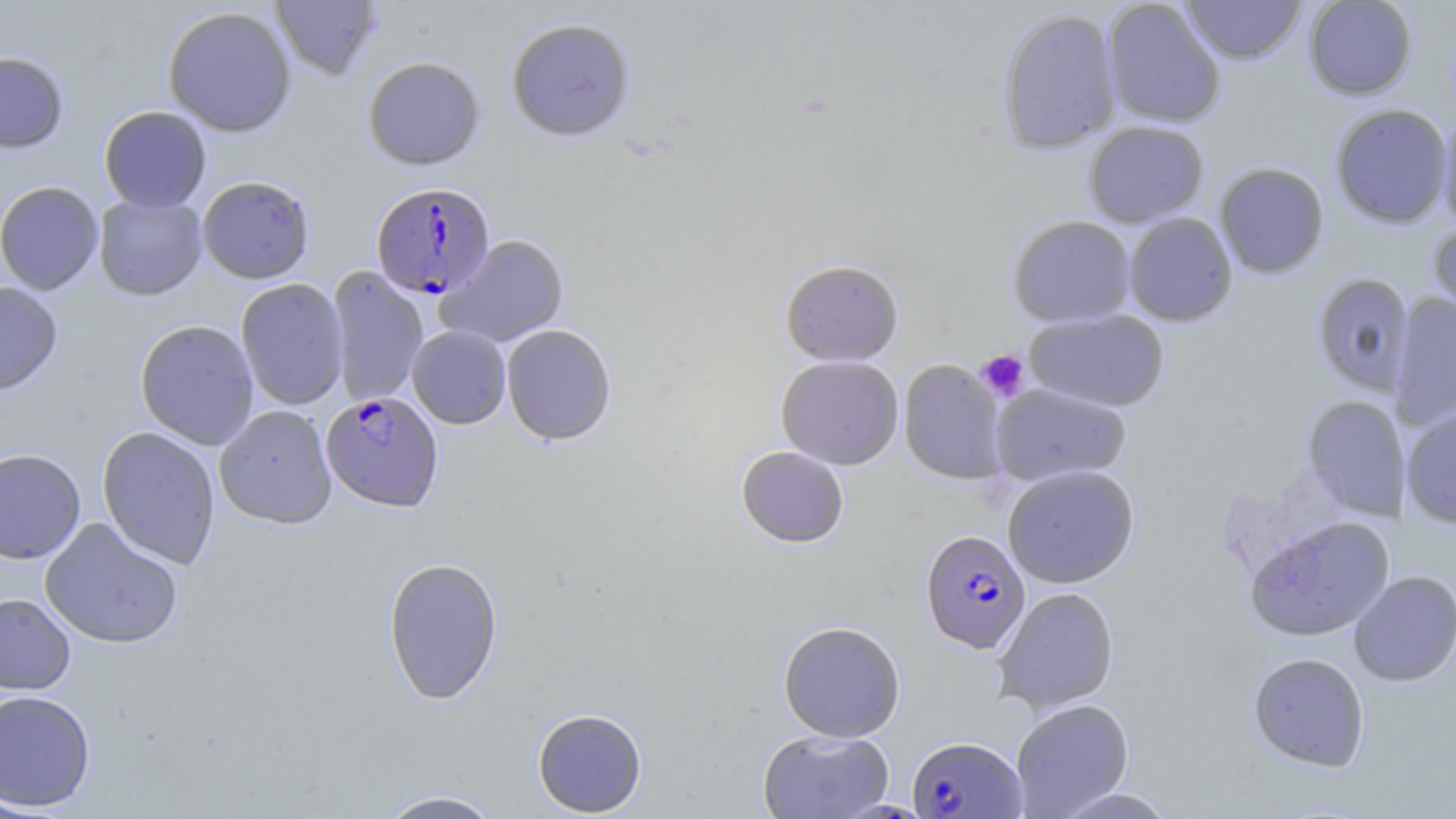
Summary:
  - Coordinate format: approximate bounding boxes as named x1/y1/x2/y2 corners in pixels
  - Plasmodium falciparum-infected red blood cell locations: (x1=370, y1=182, x2=496, y2=300), (x1=320, y1=391, x2=444, y2=513), (x1=920, y1=529, x2=1030, y2=654), (x1=907, y1=735, x2=1026, y2=818)
  - Uninfected red blood cell locations: (x1=270, y1=0, x2=382, y2=81), (x1=1181, y1=0, x2=1306, y2=65), (x1=1303, y1=0, x2=1417, y2=100), (x1=1102, y1=1, x2=1226, y2=129), (x1=162, y1=6, x2=297, y2=138), (x1=997, y1=8, x2=1122, y2=155), (x1=506, y1=17, x2=636, y2=143), (x1=0, y1=51, x2=70, y2=154), (x1=362, y1=55, x2=486, y2=171), (x1=1329, y1=104, x2=1453, y2=229), (x1=98, y1=106, x2=212, y2=213), (x1=1436, y1=109, x2=1456, y2=234), (x1=1083, y1=120, x2=1210, y2=228), (x1=1214, y1=162, x2=1329, y2=278), (x1=197, y1=176, x2=315, y2=285), (x1=0, y1=181, x2=103, y2=295), (x1=93, y1=194, x2=207, y2=302), (x1=1123, y1=212, x2=1238, y2=327), (x1=1008, y1=215, x2=1136, y2=327), (x1=1427, y1=223, x2=1456, y2=336), (x1=437, y1=234, x2=570, y2=349), (x1=780, y1=259, x2=904, y2=366), (x1=326, y1=267, x2=429, y2=408), (x1=1312, y1=272, x2=1414, y2=395), (x1=236, y1=279, x2=349, y2=411), (x1=0, y1=282, x2=63, y2=397), (x1=1389, y1=292, x2=1456, y2=431), (x1=1024, y1=308, x2=1171, y2=413), (x1=135, y1=320, x2=259, y2=450), (x1=501, y1=324, x2=617, y2=446), (x1=407, y1=325, x2=511, y2=429), (x1=776, y1=355, x2=904, y2=469), (x1=898, y1=359, x2=1008, y2=485), (x1=990, y1=382, x2=1132, y2=486), (x1=1301, y1=395, x2=1407, y2=520), (x1=1401, y1=404, x2=1456, y2=527), (x1=214, y1=405, x2=337, y2=529), (x1=96, y1=426, x2=221, y2=570), (x1=736, y1=446, x2=849, y2=548), (x1=0, y1=448, x2=85, y2=564), (x1=1002, y1=464, x2=1140, y2=588), (x1=1245, y1=515, x2=1395, y2=641), (x1=40, y1=518, x2=184, y2=649), (x1=382, y1=556, x2=504, y2=705), (x1=1348, y1=570, x2=1456, y2=687), (x1=992, y1=586, x2=1120, y2=717), (x1=0, y1=593, x2=76, y2=694), (x1=778, y1=621, x2=906, y2=742), (x1=1247, y1=652, x2=1370, y2=772), (x1=0, y1=689, x2=96, y2=812), (x1=1010, y1=699, x2=1134, y2=818), (x1=532, y1=708, x2=647, y2=817), (x1=757, y1=728, x2=894, y2=818), (x1=1050, y1=786, x2=1180, y2=819), (x1=374, y1=789, x2=505, y2=818)
  - Platelet locations: (x1=976, y1=349, x2=1030, y2=402)
  - Slide-level diagnosis: Plasmodium falciparum
  - Stain: May-Grünwald-Giemsa
  - Modality: optical microscopy
  - Magnification: 1000x
  - Preparation: thin blood film
  - Image size: 1456×819 pixels
  - Field of view: one of a larger specimen